Report the malaria status of this cell.
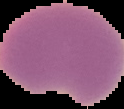

It is parasitized.

Summary:
  - Image size: 124×109 pixels
  - Image type: segmented cell region with the area outside set to black
  - Preparation: thin blood smear